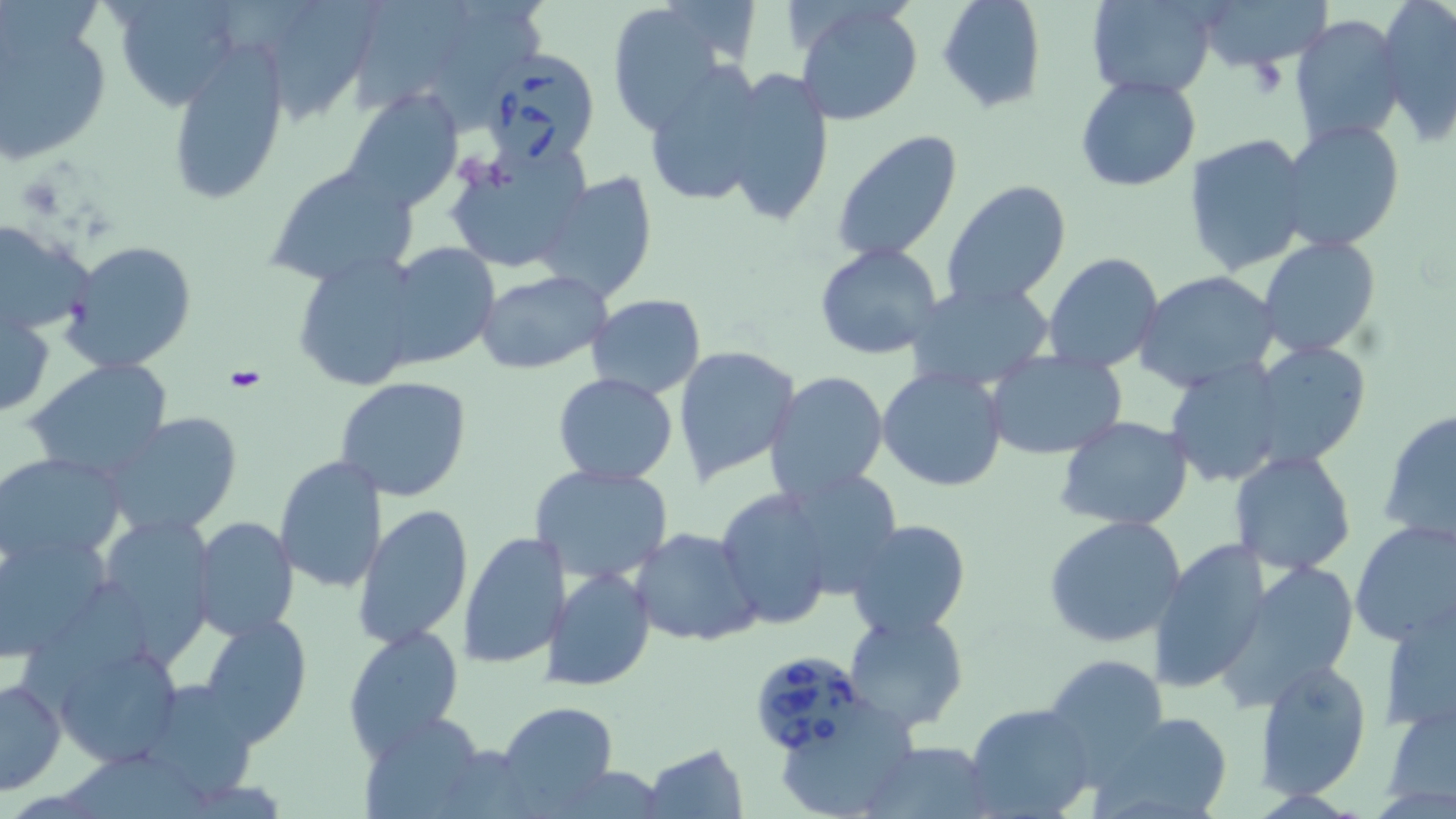

Summary:
  - Coordinate format: approximate bounding boxes as [x1, y1, x2, y2] in pixels
  - Uninfected red blood cell locations: [110, 0, 242, 110], [937, 0, 1045, 115], [1086, 0, 1218, 99], [1192, 0, 1330, 69], [1374, 0, 1456, 140], [285, 1, 389, 123], [606, 1, 737, 134], [363, 4, 465, 112], [793, 4, 923, 127], [0, 9, 114, 165], [1289, 14, 1406, 147], [164, 44, 290, 205], [642, 66, 771, 210], [722, 66, 834, 228], [1075, 75, 1202, 191], [340, 89, 464, 212], [1277, 120, 1404, 253], [832, 131, 961, 263], [1184, 133, 1313, 276], [445, 147, 589, 273], [262, 160, 418, 286], [533, 172, 659, 304], [940, 178, 1072, 310], [0, 220, 94, 340], [1258, 236, 1383, 358], [60, 240, 198, 374], [378, 242, 499, 368], [813, 243, 946, 362], [1043, 251, 1165, 373], [290, 253, 425, 393], [475, 270, 611, 375], [1133, 270, 1281, 392], [903, 278, 1056, 391], [587, 293, 707, 398], [1, 302, 54, 418], [1247, 341, 1373, 470], [673, 345, 800, 483], [984, 349, 1129, 460], [1161, 356, 1290, 488], [23, 358, 173, 481], [877, 367, 1007, 493], [764, 371, 890, 502], [552, 373, 679, 485], [333, 376, 477, 503], [1378, 409, 1456, 548], [102, 412, 242, 538], [1054, 417, 1194, 531], [1229, 449, 1359, 575], [0, 451, 127, 568], [275, 455, 386, 596], [529, 463, 675, 585], [716, 487, 841, 631], [351, 503, 474, 653], [107, 511, 224, 685], [1043, 515, 1188, 649], [188, 516, 298, 640], [844, 519, 972, 641], [1349, 520, 1456, 648], [630, 526, 766, 648], [0, 528, 117, 659], [458, 532, 569, 669], [1149, 536, 1273, 696], [1211, 561, 1362, 713], [545, 566, 656, 690], [24, 583, 155, 706], [1377, 606, 1456, 735], [843, 610, 968, 734], [197, 612, 314, 746], [343, 626, 464, 760], [47, 635, 184, 769], [1044, 653, 1168, 770], [1255, 658, 1373, 800], [1, 675, 67, 794], [142, 682, 264, 799], [1381, 697, 1456, 811], [497, 702, 618, 813], [782, 702, 923, 817], [966, 703, 1099, 819], [358, 710, 487, 817], [1087, 710, 1237, 819], [863, 741, 997, 818], [641, 743, 750, 818]
  - Platelet locations: [1243, 56, 1290, 100]
  - Babesia divergens-infected red blood cell locations: [475, 49, 603, 169], [756, 654, 865, 760]
  - Slide-level diagnosis: Babesia divergens
  - Modality: optical microscopy
  - Stain: May-Grünwald-Giemsa
  - Image size: 1456×819 pixels
  - Magnification: 1000x
  - Preparation: thin blood smear
  - Field of view: one of a larger specimen